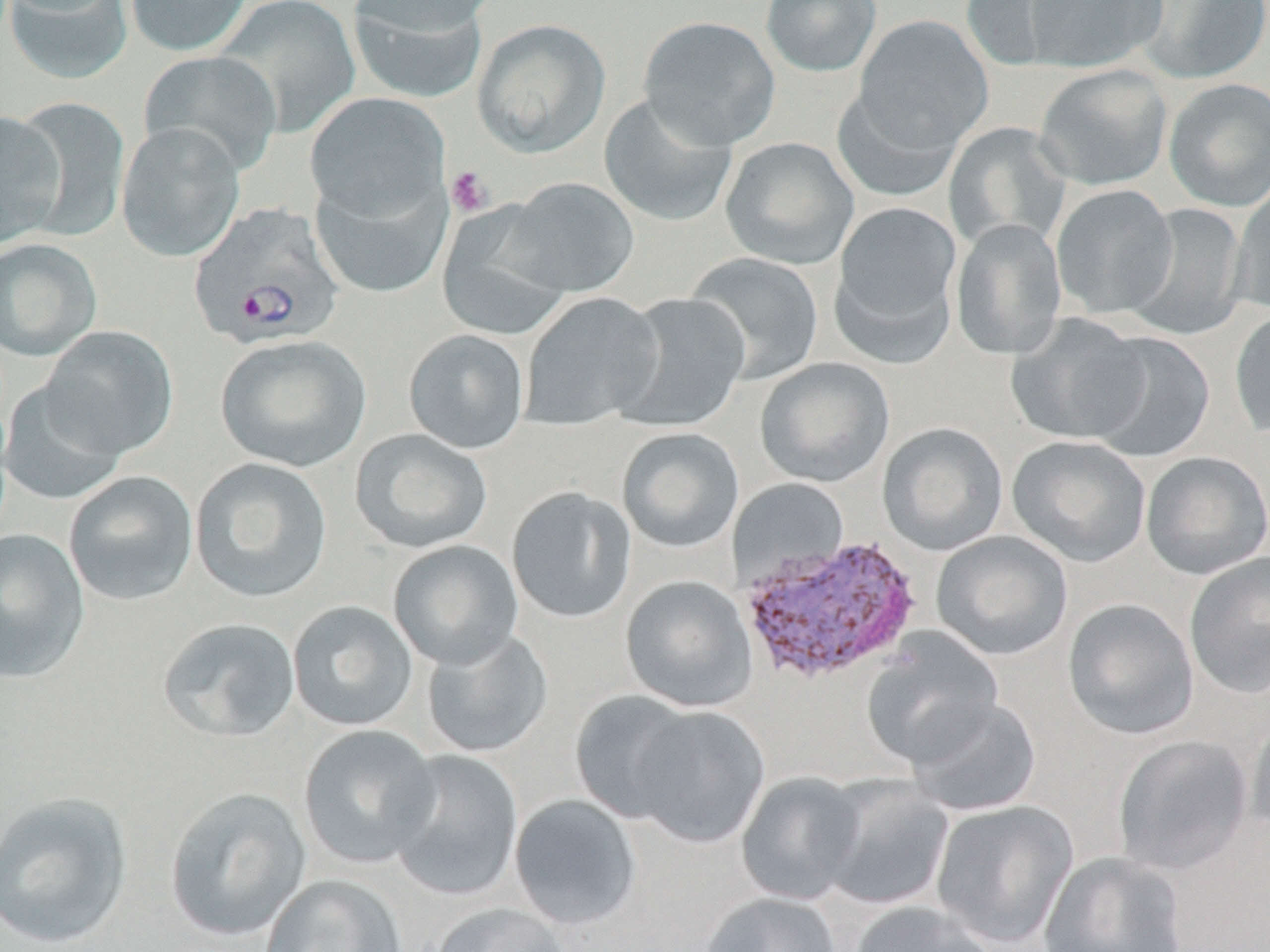

Summary:
  - Coordinate format: approximate bounding boxes as [x1, y1, x2, y2] in pixels
  - Plasmodium vivax-infected red blood cell locations: [188, 202, 344, 351], [738, 534, 923, 684]
  - Platelet locations: [444, 165, 494, 217]
  - Uninfected red blood cell locations: [3, 0, 134, 84], [124, 0, 252, 57], [214, 0, 360, 138], [346, 0, 492, 102], [347, 0, 500, 38], [760, 0, 882, 77], [959, 0, 1088, 72], [1022, 0, 1167, 73], [1130, 1, 1270, 84], [638, 15, 781, 151], [854, 15, 994, 153], [471, 18, 611, 158], [138, 49, 282, 177], [1033, 64, 1173, 190], [1163, 78, 1270, 212], [830, 86, 962, 202], [304, 92, 450, 222], [599, 92, 738, 227], [13, 96, 130, 241], [0, 110, 66, 249], [116, 121, 246, 263], [944, 122, 1072, 251], [720, 136, 858, 270], [310, 171, 451, 299], [500, 177, 640, 298], [1232, 179, 1270, 315], [1050, 184, 1178, 320], [831, 201, 963, 347], [1124, 203, 1249, 342], [437, 205, 572, 341], [949, 218, 1068, 360], [0, 238, 102, 361], [684, 252, 825, 385], [518, 292, 665, 431], [612, 292, 751, 433], [1229, 306, 1270, 440], [1005, 313, 1151, 446], [40, 325, 178, 459], [404, 329, 530, 454], [1086, 331, 1216, 463], [215, 333, 371, 472], [754, 357, 895, 489], [1, 380, 128, 505], [877, 422, 1009, 557], [616, 427, 744, 553], [350, 428, 493, 554], [1006, 435, 1152, 568], [1141, 451, 1270, 580], [190, 457, 332, 603], [64, 471, 198, 606], [727, 479, 850, 586], [506, 486, 637, 624], [0, 527, 89, 683], [931, 530, 1074, 662], [387, 539, 524, 671], [1183, 551, 1270, 699], [620, 575, 757, 712], [1063, 598, 1199, 740], [287, 600, 418, 731], [157, 617, 301, 743], [421, 628, 553, 758], [860, 629, 1004, 768], [570, 690, 702, 824], [906, 696, 1041, 817], [627, 704, 770, 848], [1245, 707, 1270, 841], [298, 724, 441, 869], [1112, 734, 1254, 877], [385, 749, 525, 903], [735, 771, 867, 906], [818, 779, 954, 912], [163, 786, 312, 943], [0, 790, 134, 949], [508, 794, 642, 930], [930, 800, 1079, 949], [1038, 850, 1188, 952], [260, 874, 408, 952], [700, 891, 841, 952], [849, 900, 998, 952], [429, 902, 572, 952]
  - Slide-level diagnosis: Plasmodium vivax
  - Preparation: thin blood smear
  - Magnification: 1000x
  - Image size: 1270×952 pixels
  - Field of view: one of a larger specimen
  - Stain: May-Grünwald-Giemsa
  - Modality: light microscopy